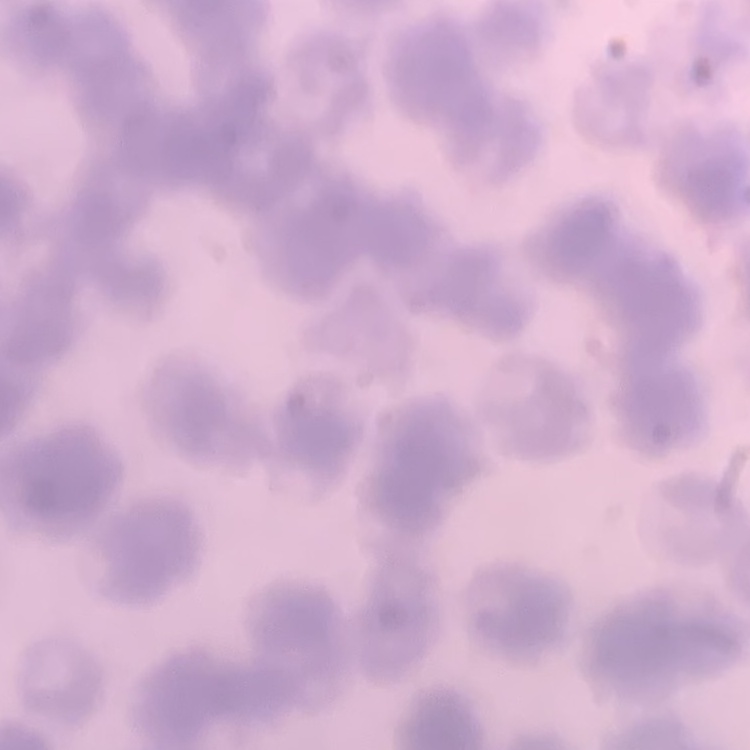

erythrocyte morphology = rouleaux formation
image type = one tile cut from a larger photomicrograph
stain = Field's or Giemsa
preparation = thin blood smear